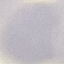
Summary:
  - Result: negative for malaria parasites
  - Stain: Giemsa
  - Preparation: thin blood smear
  - Image type: automatically extracted cell patch, resized to 64 × 64 pixels
  - Capture: smartphone through the microscope eyepiece